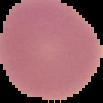
preparation: thin blood smear
image_size: 103×103 pixels
result: negative for malaria parasites
image_type: cell region segmented out of the field of view; surrounding area masked to black